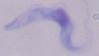
identification: trypanosome
modality: photomicrograph
magnification: 1000x